Outline each blood parasite and name the species.
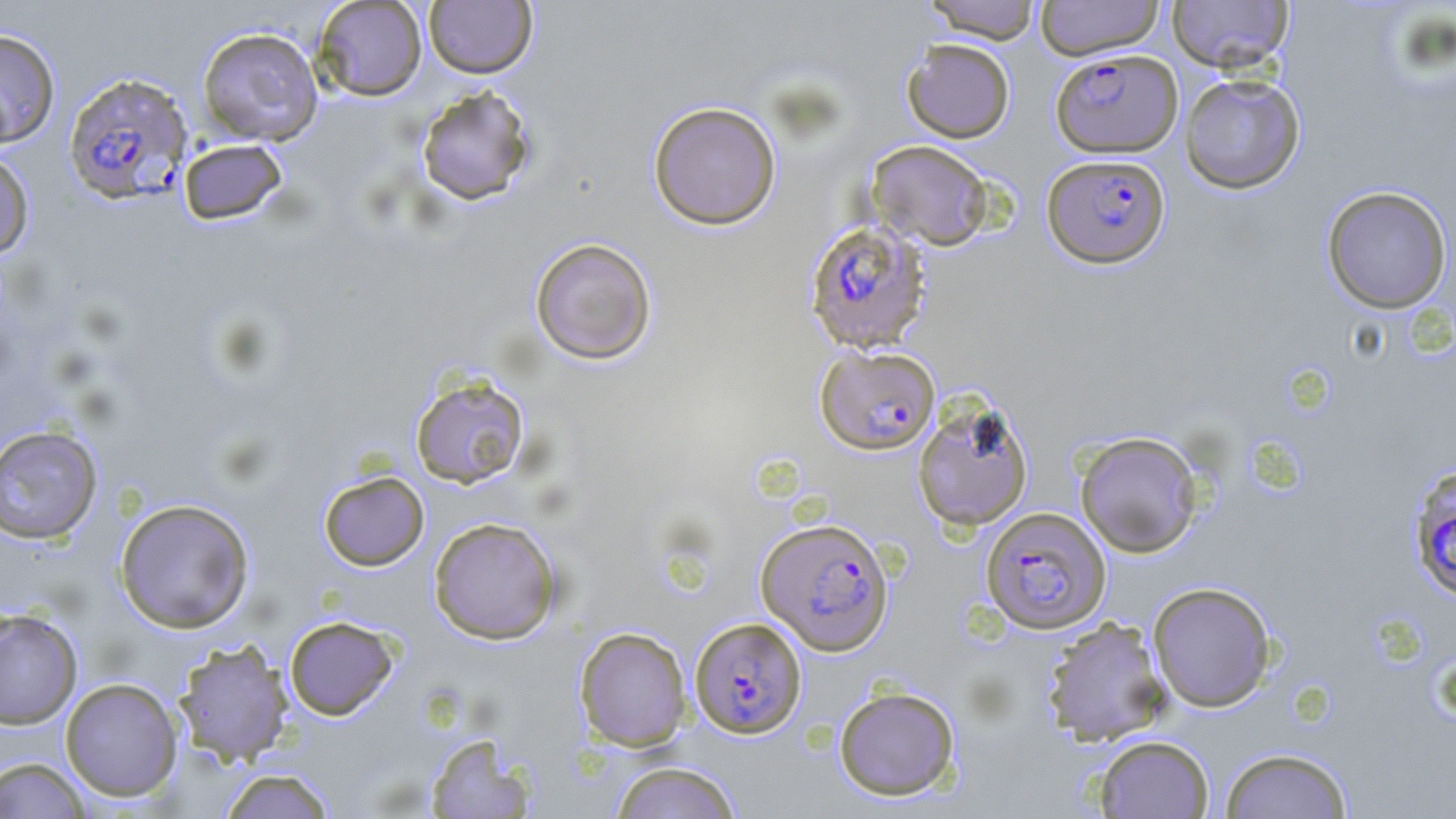

Approximate bounding boxes as (x1,y1)-(x2,y2) corner pairs in pixels.
Plasmodium falciparum-infected red blood cells: (1050,48)-(1183,158), (63,72)-(194,206), (1042,153)-(1171,269), (804,221)-(932,354), (813,339)-(940,450), (1407,464)-(1456,603), (980,507)-(1111,634), (756,517)-(894,656), (689,616)-(807,739).
No Plasmodium ovale, Plasmodium malariae, Plasmodium vivax, Babesia divergens, or Trypanosoma brucei observed.

{
  "slide_level_diagnosis": "Plasmodium falciparum",
  "image_size": "1456×819 pixels",
  "modality": "light microscopy",
  "stain": "May-Grünwald-Giemsa",
  "magnification": "1000x",
  "preparation": "thin blood smear",
  "field_of_view": "one of a larger specimen",
  "uninfected_red_blood_cell_locations": "approximate bounding boxes as (x1,y1)-(x2,y2) corner pairs in pixels: (312,0)-(428,101), (922,0)-(1042,44), (1035,0)-(1164,60), (1167,0)-(1294,73), (423,1)-(537,78), (196,27)-(324,146), (0,28)-(61,147), (901,38)-(1015,143), (1179,73)-(1305,194), (415,84)-(537,207), (648,100)-(782,230), (178,138)-(289,225), (866,140)-(994,251), (0,150)-(35,260), (1321,185)-(1453,314), (530,237)-(657,365), (410,375)-(530,489), (913,399)-(1034,530), (0,425)-(103,544), (1075,432)-(1204,558), (318,470)-(430,572), (114,498)-(255,633), (428,516)-(562,645), (1147,581)-(1276,712), (0,608)-(83,730), (284,616)-(399,720), (1041,617)-(1172,746), (574,626)-(693,750), (173,639)-(294,767), (60,677)-(184,802), (833,685)-(961,801), (424,733)-(537,817), (1092,734)-(1214,818), (1219,746)-(1354,818), (1,757)-(93,817), (609,760)-(742,819), (217,768)-(338,818)"
}